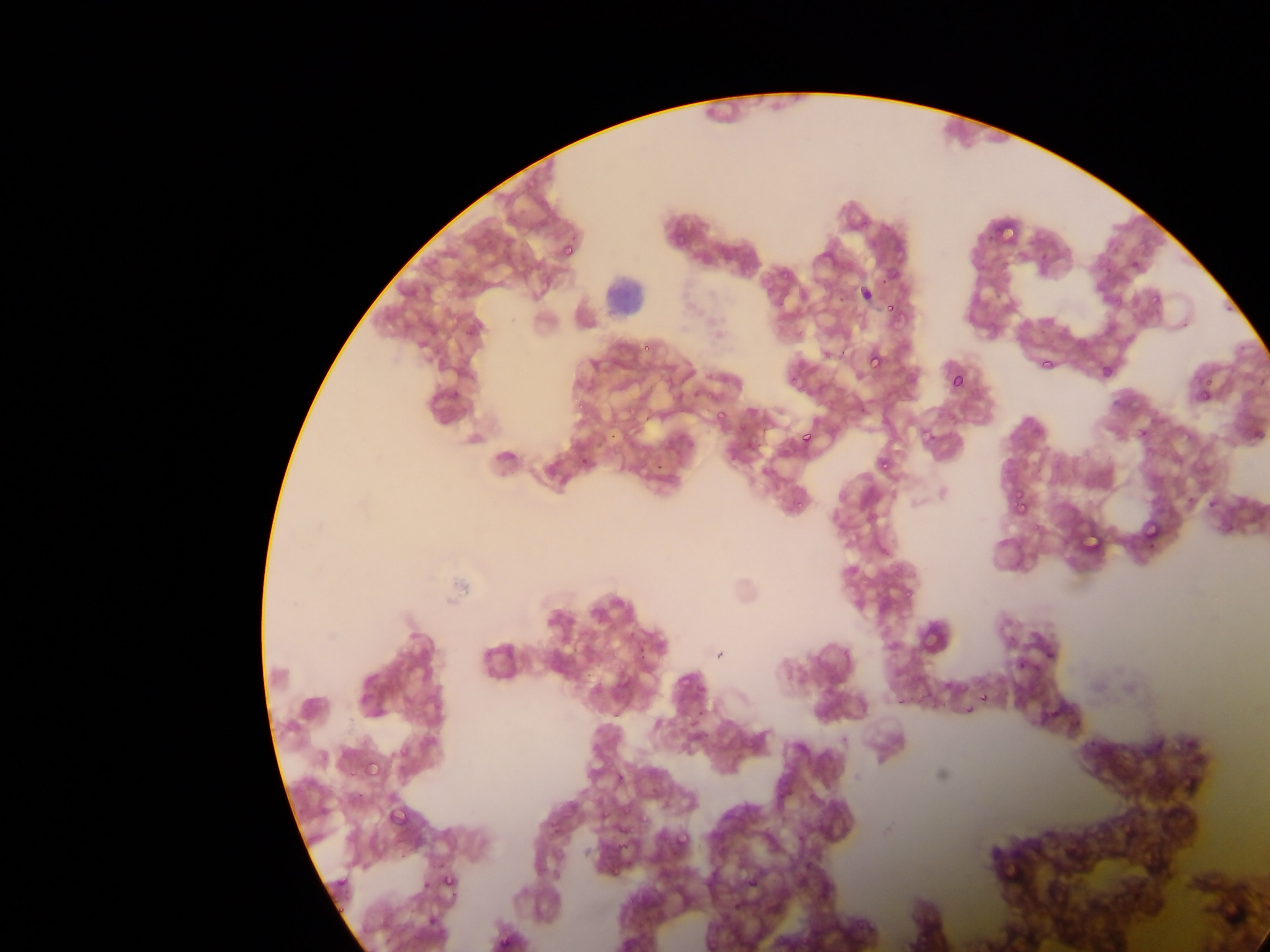
{
  "country": "Ghana",
  "image_size": "1270×952 pixels",
  "leukocyte_locations": "approximate bounding boxes as left top right bottom in pixels: 604 276 648 318",
  "capture": "mobile-phone photograph through a microscope",
  "field_of_view": "single",
  "plasmodium_parasite_locations": "approximate bounding boxes as left top right bottom in pixels: 998 218 1022 243; 675 226 688 247; 559 238 581 263; 881 261 900 291; 853 278 868 300; 1150 290 1165 307; 883 298 897 313; 640 334 659 352; 865 348 887 373; 1099 357 1121 376; 1044 358 1054 372; 947 372 966 392; 1202 374 1217 392; 1198 386 1214 404; 573 387 595 412; 714 405 730 421; 608 425 625 444; 1135 425 1152 445; 797 427 816 449; 577 448 597 469; 874 454 894 477; 653 463 667 476; 1012 480 1026 502; 1013 497 1034 515; 1203 499 1219 511; 1138 513 1157 537; 1217 519 1235 532; 1080 529 1102 548; 1142 540 1162 551; 904 585 920 603; 917 624 948 654; 1015 657 1031 672; 612 668 635 695; 977 688 993 702; 687 707 707 730; 394 742 415 765; 362 756 386 784; 386 804 411 831; 671 831 690 853; 439 871 460 893",
  "preparation": "thin blood smear"
}